Outline each uninfected red blood cell.
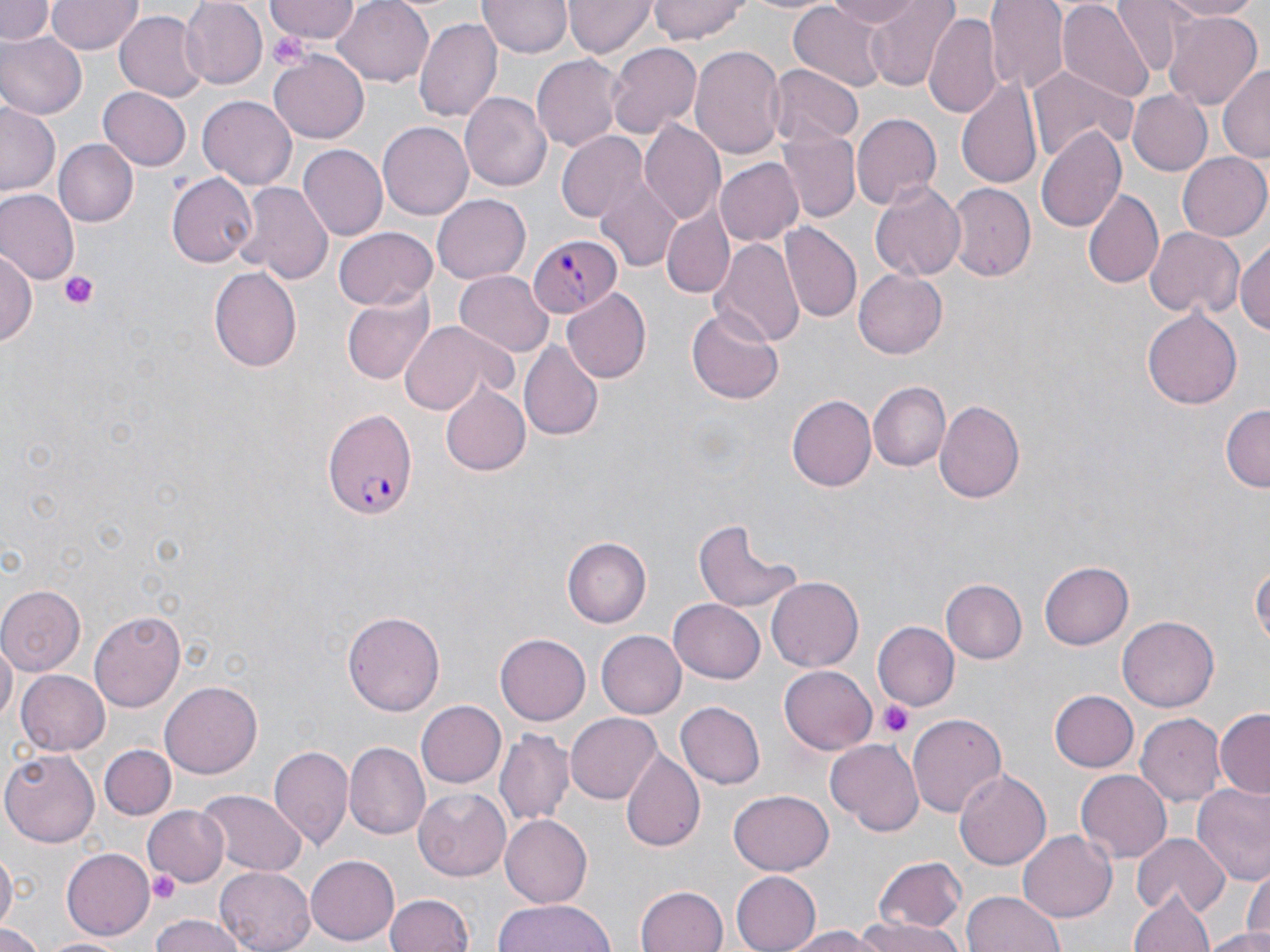
Approximate bounding boxes as named x1/y1/x2/y2 corners in pixels.
Uninfected red blood cells: (x1=0, y1=0, x2=56, y2=44), (x1=46, y1=0, x2=141, y2=55), (x1=181, y1=0, x2=269, y2=87), (x1=264, y1=0, x2=361, y2=43), (x1=333, y1=0, x2=437, y2=88), (x1=478, y1=0, x2=572, y2=58), (x1=565, y1=0, x2=656, y2=58), (x1=646, y1=0, x2=751, y2=43), (x1=735, y1=0, x2=838, y2=16), (x1=825, y1=0, x2=923, y2=30), (x1=863, y1=0, x2=959, y2=91), (x1=985, y1=0, x2=1069, y2=96), (x1=1162, y1=0, x2=1265, y2=20), (x1=1056, y1=1, x2=1154, y2=104), (x1=1114, y1=1, x2=1195, y2=77), (x1=787, y1=3, x2=888, y2=92), (x1=114, y1=9, x2=205, y2=104), (x1=924, y1=10, x2=1000, y2=116), (x1=1165, y1=10, x2=1262, y2=112), (x1=416, y1=16, x2=503, y2=124), (x1=0, y1=33, x2=86, y2=120), (x1=607, y1=42, x2=702, y2=141), (x1=690, y1=42, x2=787, y2=161), (x1=269, y1=50, x2=369, y2=142), (x1=533, y1=53, x2=625, y2=154), (x1=1027, y1=64, x2=1137, y2=165), (x1=1218, y1=64, x2=1270, y2=164), (x1=768, y1=65, x2=864, y2=147), (x1=958, y1=74, x2=1043, y2=192), (x1=98, y1=88, x2=192, y2=171), (x1=1126, y1=89, x2=1211, y2=175), (x1=460, y1=92, x2=552, y2=191), (x1=197, y1=93, x2=295, y2=187), (x1=0, y1=99, x2=62, y2=201), (x1=851, y1=113, x2=942, y2=210), (x1=642, y1=120, x2=726, y2=223), (x1=378, y1=123, x2=472, y2=220), (x1=1037, y1=125, x2=1126, y2=234), (x1=557, y1=132, x2=646, y2=222), (x1=778, y1=132, x2=859, y2=222), (x1=57, y1=139, x2=139, y2=228), (x1=296, y1=146, x2=386, y2=240), (x1=1177, y1=150, x2=1270, y2=242), (x1=715, y1=159, x2=804, y2=247), (x1=168, y1=173, x2=257, y2=269), (x1=595, y1=179, x2=681, y2=270), (x1=868, y1=179, x2=967, y2=282), (x1=236, y1=181, x2=334, y2=284), (x1=948, y1=185, x2=1037, y2=281), (x1=1082, y1=188, x2=1164, y2=288), (x1=0, y1=189, x2=78, y2=284), (x1=433, y1=194, x2=531, y2=282), (x1=661, y1=208, x2=734, y2=299), (x1=781, y1=222, x2=860, y2=321), (x1=333, y1=226, x2=436, y2=310), (x1=1144, y1=226, x2=1244, y2=321), (x1=1235, y1=235, x2=1270, y2=339), (x1=712, y1=237, x2=804, y2=347), (x1=1, y1=246, x2=37, y2=352), (x1=208, y1=266, x2=302, y2=372), (x1=854, y1=269, x2=948, y2=359), (x1=453, y1=271, x2=552, y2=356), (x1=341, y1=290, x2=436, y2=385), (x1=565, y1=290, x2=651, y2=382), (x1=686, y1=306, x2=786, y2=405), (x1=1144, y1=308, x2=1243, y2=409), (x1=398, y1=321, x2=505, y2=416), (x1=519, y1=341, x2=604, y2=442), (x1=869, y1=381, x2=952, y2=472), (x1=437, y1=383, x2=530, y2=476), (x1=787, y1=395, x2=876, y2=491), (x1=933, y1=399, x2=1026, y2=506), (x1=1222, y1=404, x2=1270, y2=492), (x1=691, y1=518, x2=802, y2=616), (x1=563, y1=537, x2=651, y2=627), (x1=1251, y1=556, x2=1269, y2=663), (x1=1040, y1=562, x2=1134, y2=650), (x1=769, y1=576, x2=863, y2=670), (x1=943, y1=579, x2=1026, y2=663), (x1=0, y1=586, x2=85, y2=675), (x1=671, y1=597, x2=765, y2=682), (x1=344, y1=610, x2=444, y2=719), (x1=89, y1=611, x2=184, y2=714), (x1=1119, y1=616, x2=1217, y2=713), (x1=871, y1=622, x2=957, y2=711), (x1=595, y1=630, x2=687, y2=719), (x1=496, y1=634, x2=591, y2=726), (x1=591, y1=636, x2=709, y2=777), (x1=1, y1=637, x2=16, y2=727), (x1=780, y1=665, x2=878, y2=755), (x1=16, y1=670, x2=109, y2=755), (x1=160, y1=683, x2=263, y2=777), (x1=1051, y1=690, x2=1139, y2=771), (x1=676, y1=700, x2=765, y2=788), (x1=416, y1=702, x2=506, y2=787), (x1=1215, y1=710, x2=1269, y2=798), (x1=908, y1=712, x2=1008, y2=817), (x1=566, y1=713, x2=662, y2=805), (x1=1136, y1=713, x2=1225, y2=803), (x1=495, y1=727, x2=573, y2=824), (x1=825, y1=740, x2=923, y2=835), (x1=343, y1=743, x2=430, y2=840), (x1=101, y1=745, x2=175, y2=819), (x1=267, y1=746, x2=353, y2=848), (x1=619, y1=749, x2=705, y2=853), (x1=2, y1=750, x2=100, y2=846), (x1=955, y1=767, x2=1051, y2=872), (x1=1075, y1=770, x2=1171, y2=862), (x1=1193, y1=784, x2=1270, y2=890), (x1=414, y1=788, x2=513, y2=880), (x1=197, y1=789, x2=305, y2=877), (x1=730, y1=790, x2=834, y2=875), (x1=142, y1=806, x2=231, y2=887), (x1=500, y1=814, x2=592, y2=909), (x1=1019, y1=828, x2=1116, y2=921), (x1=1133, y1=834, x2=1228, y2=916), (x1=60, y1=848, x2=154, y2=939), (x1=0, y1=850, x2=16, y2=933), (x1=306, y1=855, x2=401, y2=946), (x1=874, y1=857, x2=967, y2=933), (x1=217, y1=865, x2=316, y2=952), (x1=727, y1=870, x2=820, y2=952), (x1=635, y1=885, x2=729, y2=952), (x1=1131, y1=889, x2=1214, y2=952), (x1=963, y1=891, x2=1064, y2=952), (x1=383, y1=894, x2=473, y2=952), (x1=496, y1=897, x2=614, y2=952), (x1=147, y1=915, x2=251, y2=952), (x1=853, y1=921, x2=965, y2=952), (x1=0, y1=923, x2=49, y2=952), (x1=780, y1=926, x2=885, y2=951), (x1=1202, y1=928, x2=1270, y2=951), (x1=37, y1=935, x2=132, y2=951).

Summary:
  - Plasmodium falciparum-infected red blood cell locations: (x1=528, y1=233, x2=622, y2=319), (x1=321, y1=412, x2=418, y2=519)
  - Platelet locations: (x1=268, y1=31, x2=310, y2=69), (x1=56, y1=269, x2=103, y2=309), (x1=877, y1=698, x2=915, y2=739), (x1=147, y1=873, x2=182, y2=905)
  - Slide-level diagnosis: Plasmodium falciparum
  - Magnification: 1000x
  - Stain: May-Grünwald-Giemsa
  - Field of view: single
  - Modality: optical microscopy
  - Preparation: thin blood film
  - Image size: 1270×952 pixels